Report the malaria status of this cell.
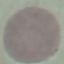

It is uninfected.

Summary:
  - Capture: smartphone through the microscope eyepiece
  - Image type: cell patch, automatically extracted from a larger field of view and resized to 64 × 64 pixels
  - Stain: Giemsa
  - Preparation: thin smear